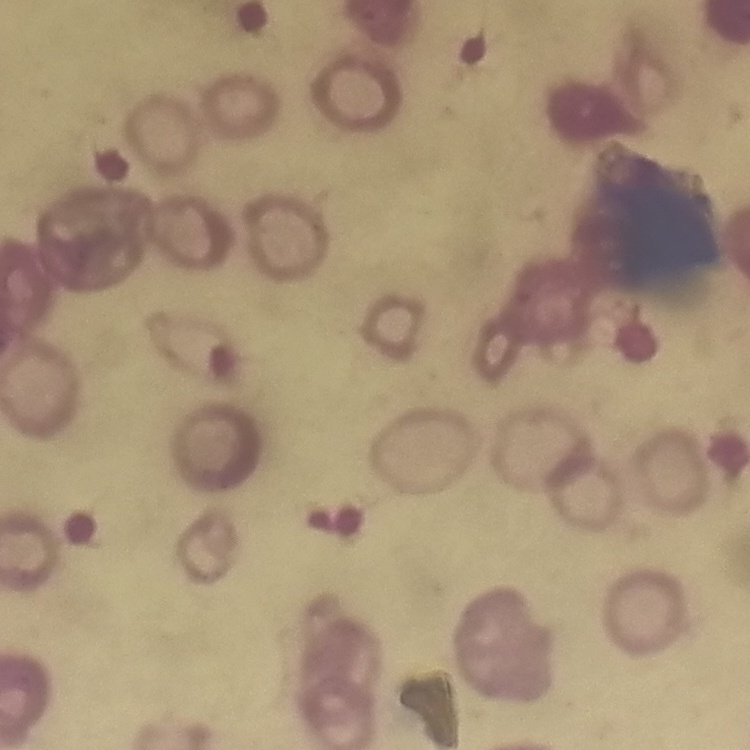
{
  "erythrocyte_morphology": "rouleaux formation",
  "stain": "Field's or Giemsa",
  "image_type": "square crop of a larger photomicrograph",
  "preparation": "thin blood smear"
}